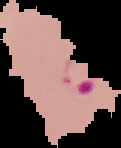
From a thin blood film. Result: Plasmodium parasites detected. Image is 121×148 pixels. The area outside the segmented cell region is set to black.